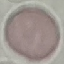

Summary:
  - Malaria status: uninfected
  - Capture: smartphone camera at the microscope eyepiece
  - Preparation: thin blood smear
  - Stain: Giemsa
  - Image type: automatically extracted cell patch, resized to 64 × 64 pixels